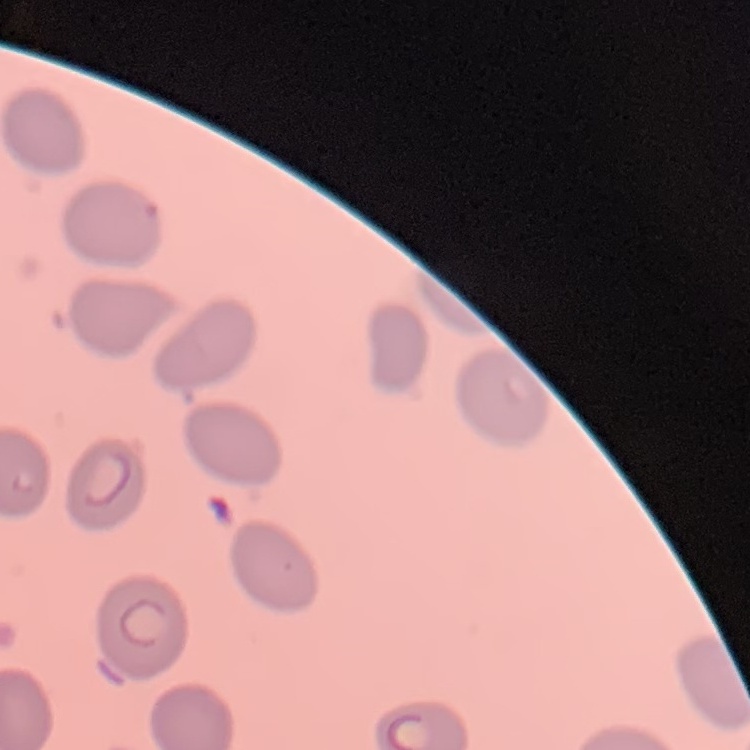
Summary:
  - Red blood cell morphology: no rouleaux formation
  - Image type: square crop of a larger photomicrograph
  - Preparation: thin blood smear
  - Stain: Field's or Giemsa